Locate every malaria parasite by life-cycle stage, and every leukocyte.
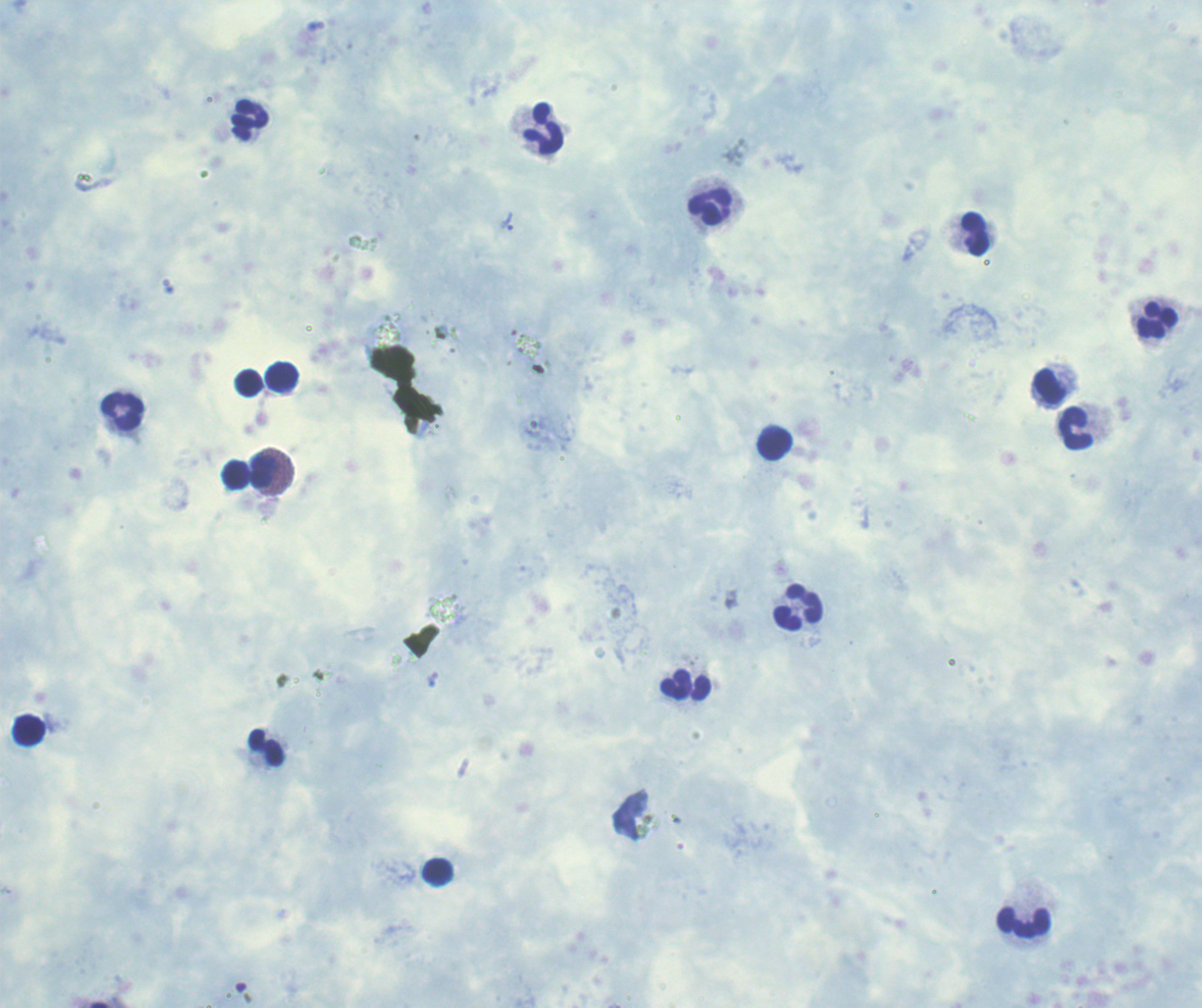

Approximate centers as {x, y} in pixels.
Trophozoites: {508, 222}.
No schizont or gametocyte forms observed.
Leukocytes: {250, 120}, {544, 129}, {710, 207}, {975, 234}, {1156, 320}, {282, 377}, {249, 383}, {1050, 388}, {122, 411}, {1076, 428}, {774, 445}, {263, 470}, {235, 474}, {799, 608}, {30, 731}, {267, 748}, {438, 872}, {1025, 920}.

Romanowsky-stained preparation. Previously used in an actual diagnosis. Captured at 100x magnification. One field from this slide. Thick blood smear. Background quality: poor. Image is 1202×1008 pixels.